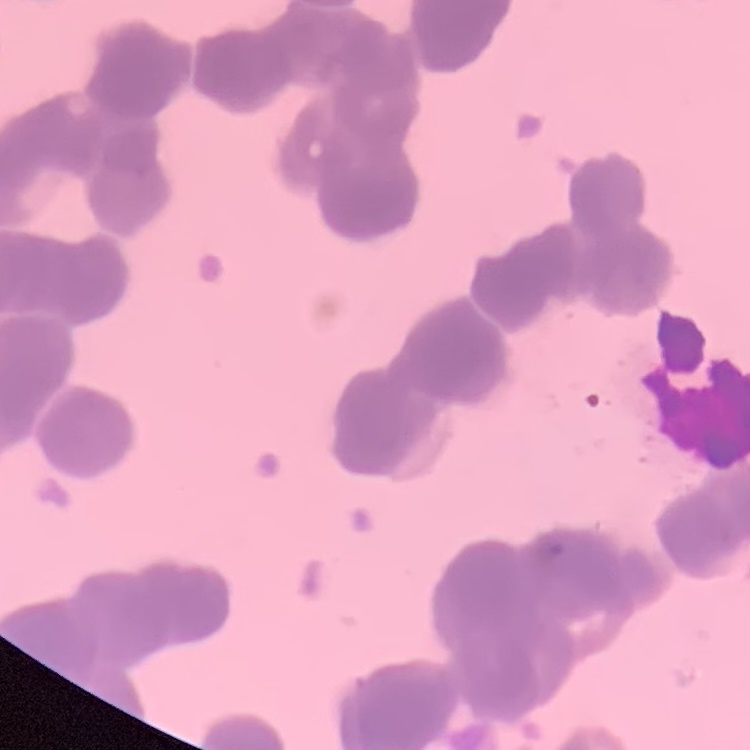

The erythrocytes show rouleaux formation. One tile cut from a larger photomicrograph. Thin blood film. Field's or Giemsa stain.